Evaluate for parasitized red blood cells.
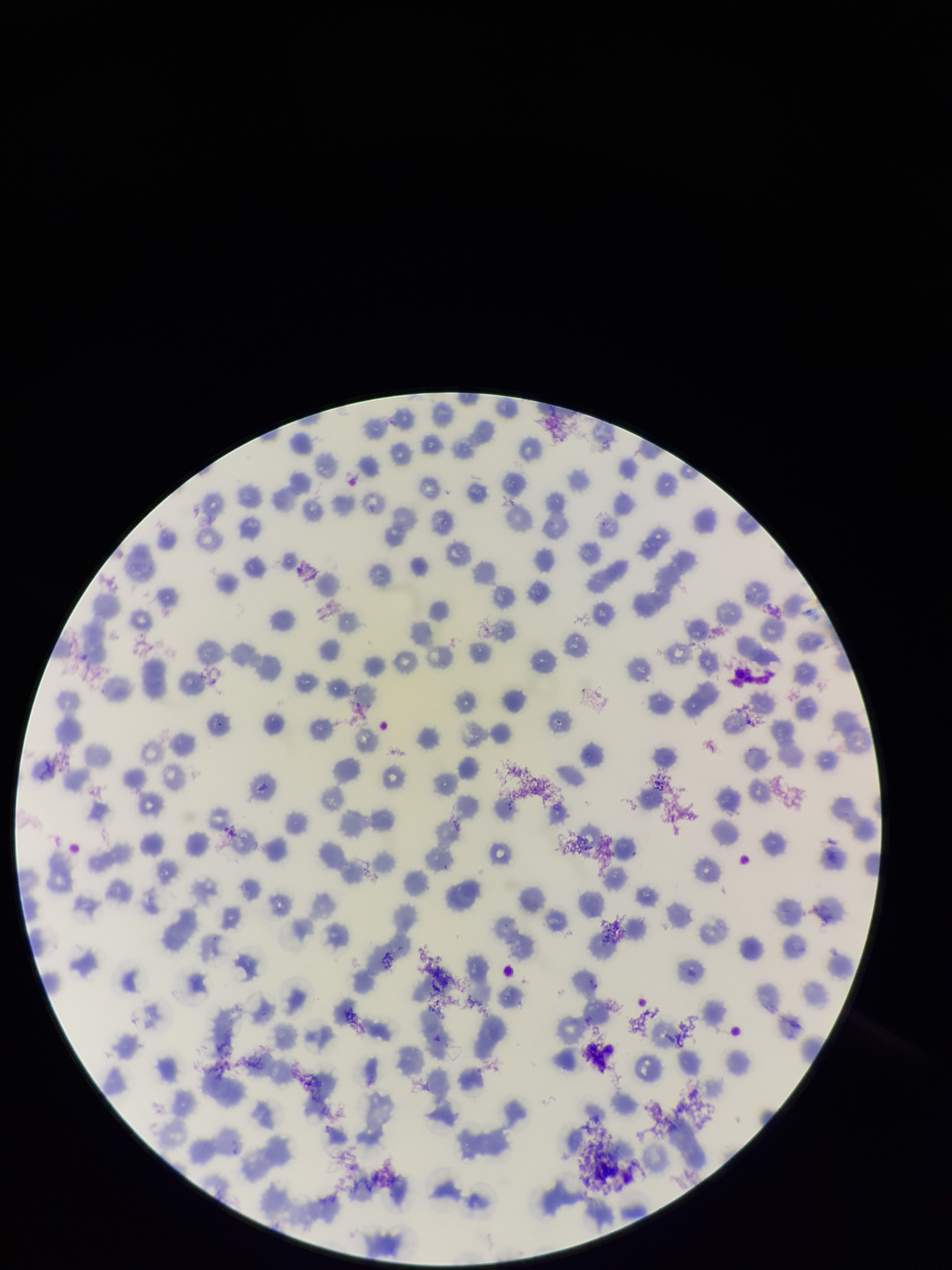

None identified.

capture = smartphone photograph through the microscope eyepiece
preparation = thin blood smear
patient malaria status = negative
parasitized red blood cell count = 0
field of view = single
image size = 952×1270 pixels
stain = Giemsa
red blood cell count = 234